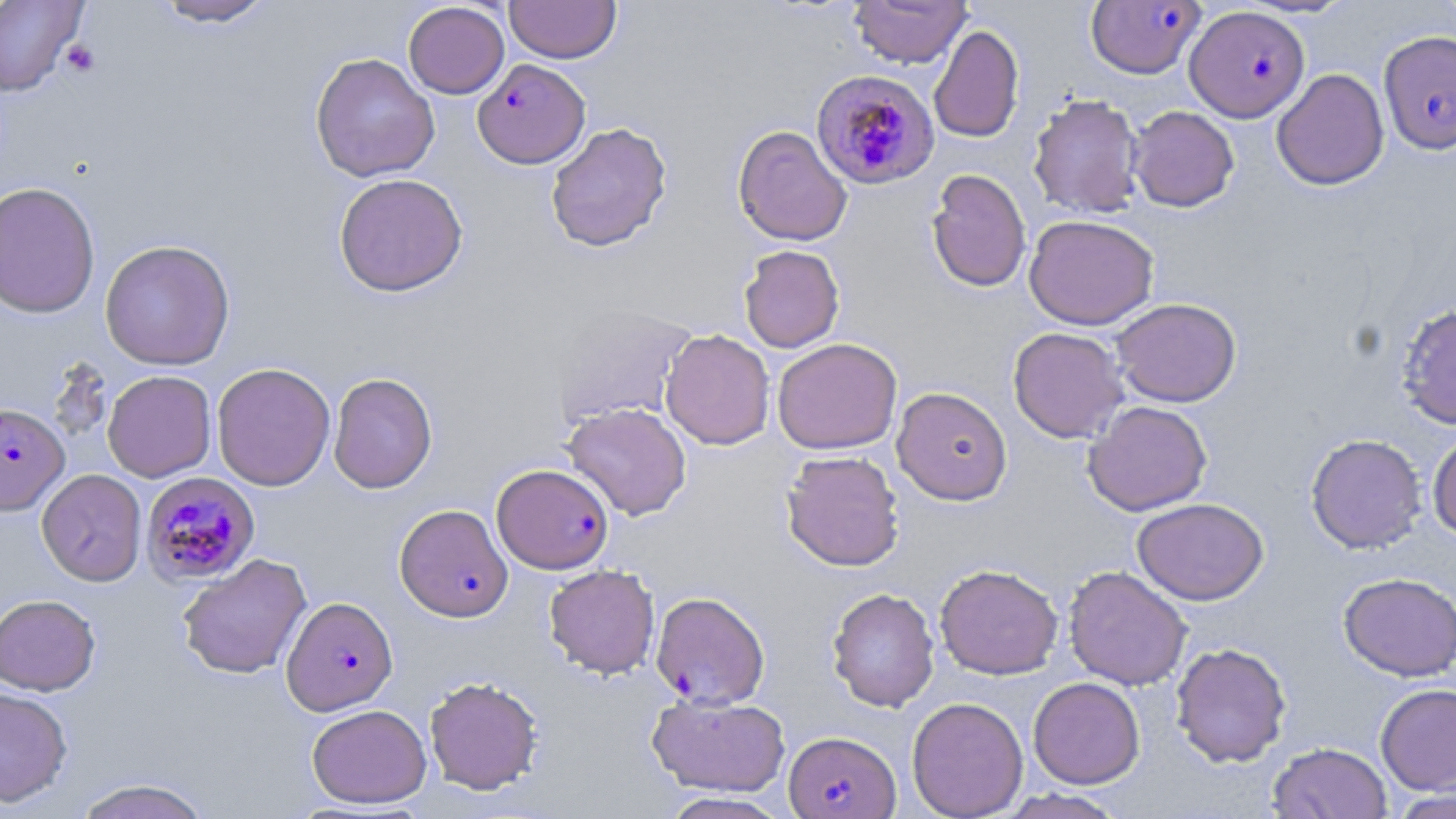

slide-level diagnosis = Plasmodium falciparum
platelet locations = approximate bounding boxes as (x1,y1)-(x2,y2) corner pairs in pixels: (60,40)-(101,77)
uninfected red blood cell locations = approximate bounding boxes as (x1,y1)-(x2,y2) corner pairs in pixels: (150,0)-(278,28), (849,0)-(971,68), (0,1)-(87,96), (504,1)-(621,63), (403,2)-(509,99), (929,24)-(1025,143), (310,52)-(440,182), (1271,68)-(1389,190), (1027,93)-(1145,219), (1128,105)-(1239,212), (545,122)-(673,252), (732,124)-(853,247), (925,168)-(1032,293), (333,173)-(468,297), (0,181)-(100,319), (1024,214)-(1159,330), (99,239)-(236,370), (739,245)-(845,353), (1111,297)-(1242,407), (1395,303)-(1456,429), (552,307)-(697,428), (1007,326)-(1129,443), (660,329)-(775,450), (772,337)-(902,455), (211,362)-(335,491), (102,370)-(217,482), (328,372)-(438,493), (891,386)-(1013,505), (1082,401)-(1213,516), (562,403)-(692,521), (1427,430)-(1456,540), (1305,433)-(1427,554), (781,450)-(905,571), (37,469)-(147,586), (1132,497)-(1269,605), (177,553)-(312,680), (934,563)-(1063,679), (543,564)-(660,679), (1063,565)-(1193,690), (1338,571)-(1456,681), (826,587)-(940,712), (0,594)-(101,696), (1171,642)-(1291,767), (424,675)-(544,795), (1028,677)-(1145,789), (1375,683)-(1456,794), (0,685)-(73,807), (646,694)-(791,796), (906,696)-(1028,818), (306,704)-(432,808), (1268,742)-(1393,818), (72,778)-(215,819), (997,788)-(1128,819), (1386,789)-(1456,818), (659,792)-(794,819)
field of view = one of a larger specimen
modality = light microscopy
preparation = thin blood smear
magnification = 1000x
Plasmodium falciparum-infected red blood cell locations = approximate bounding boxes as (x1,y1)-(x2,y2) corner pairs in pixels: (1085,1)-(1206,79), (1185,5)-(1309,122), (1379,30)-(1456,155), (472,58)-(590,168), (810,70)-(938,190), (0,403)-(70,517), (492,463)-(614,574), (139,476)-(258,591), (394,503)-(513,622), (642,595)-(762,713), (282,596)-(397,714), (784,730)-(900,818)
image size = 1456×819 pixels
stain = May-Grünwald-Giemsa